Name the blood parasite species.
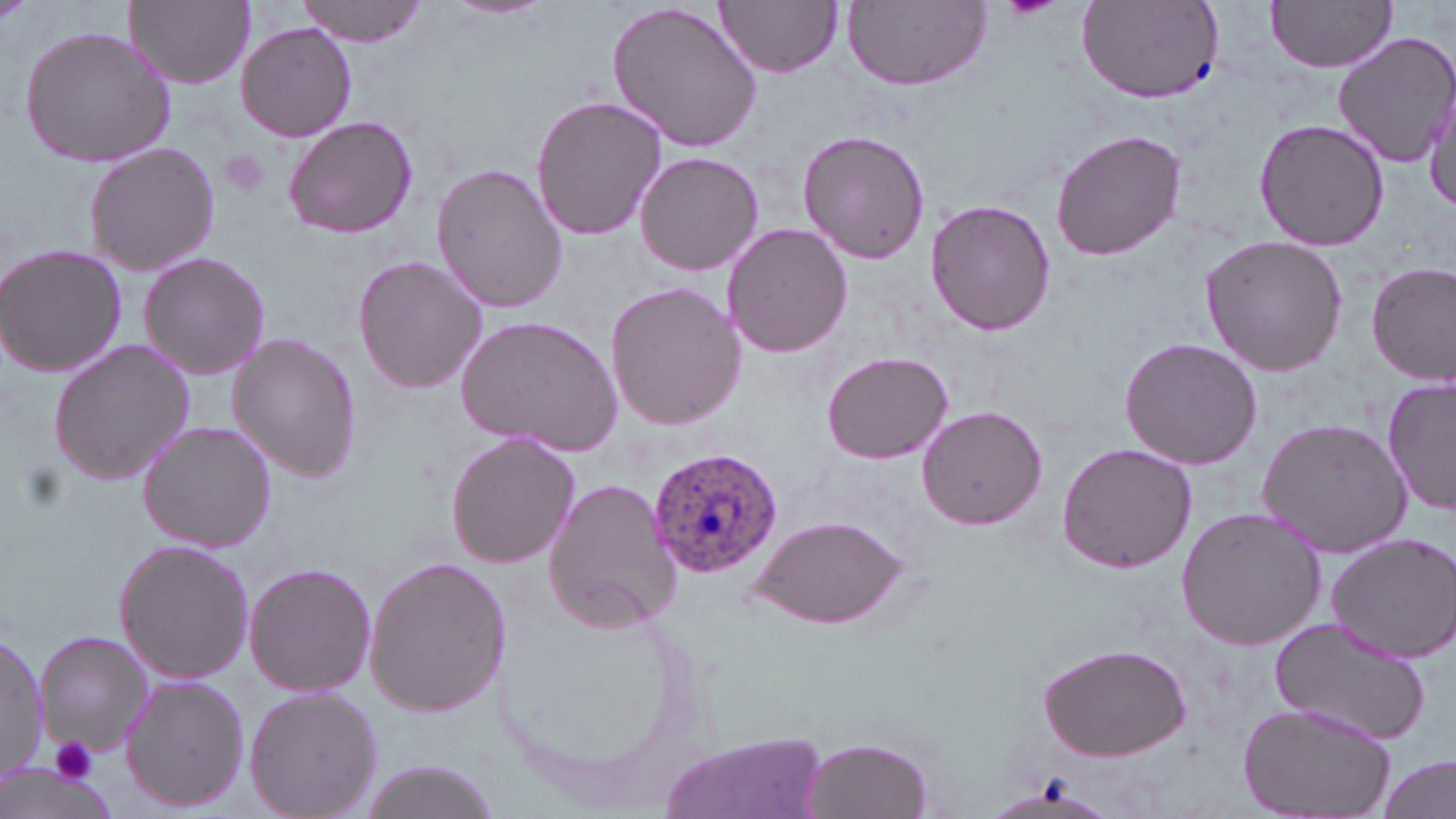
Plasmodium ovale.

Summary:
  - Coordinate format: approximate bounding boxes as (x1, y1, x2, y2) in pixels
  - Platelet locations: (218, 150, 271, 198), (47, 736, 102, 784)
  - Plasmodium ovale-infected red blood cell locations: (648, 444, 786, 577)
  - Uninfected red blood cell locations: (297, 0, 432, 46), (448, 0, 549, 21), (716, 0, 843, 77), (1267, 0, 1397, 71), (128, 1, 254, 89), (605, 1, 766, 154), (844, 1, 989, 91), (1076, 2, 1225, 102), (235, 23, 357, 141), (20, 26, 177, 170), (1332, 31, 1456, 170), (1423, 87, 1455, 212), (529, 94, 667, 241), (283, 115, 417, 240), (1253, 118, 1390, 250), (1050, 128, 1187, 261), (797, 130, 930, 265), (83, 140, 221, 276), (635, 152, 765, 277), (430, 161, 569, 314), (925, 199, 1056, 336), (720, 223, 852, 359), (1200, 235, 1349, 377), (1, 243, 127, 380), (138, 252, 270, 380), (353, 253, 489, 395), (1367, 261, 1456, 386), (605, 280, 745, 432), (458, 315, 622, 456), (228, 334, 363, 482), (1118, 336, 1266, 469), (47, 337, 196, 488), (821, 352, 954, 463), (1383, 375, 1456, 516), (917, 405, 1047, 531), (1255, 416, 1412, 559), (138, 421, 276, 553), (447, 432, 579, 569), (1055, 442, 1198, 575), (541, 475, 682, 634), (1175, 506, 1326, 652), (744, 513, 913, 631), (1326, 532, 1456, 663), (114, 540, 255, 684), (364, 556, 509, 718), (245, 562, 375, 696), (492, 584, 711, 814), (1270, 616, 1430, 745), (33, 629, 153, 757), (0, 632, 46, 787), (1036, 641, 1193, 760), (122, 675, 249, 813), (244, 685, 383, 819), (1238, 703, 1398, 819), (656, 728, 829, 819), (799, 735, 936, 819), (1378, 752, 1454, 819), (354, 760, 502, 817)
  - Stain: May-Grünwald-Giemsa
  - Modality: light microscopy
  - Image size: 1456×819 pixels
  - Field of view: single
  - Preparation: thin blood film
  - Magnification: 1000x